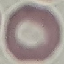 Result: negative for malaria parasites. Thin blood smear. Giemsa stain. Automatically extracted cell patch, resized to 64 × 64 pixels. Acquired by smartphone through the microscope eyepiece.